Assess the morphology of the red blood cells.
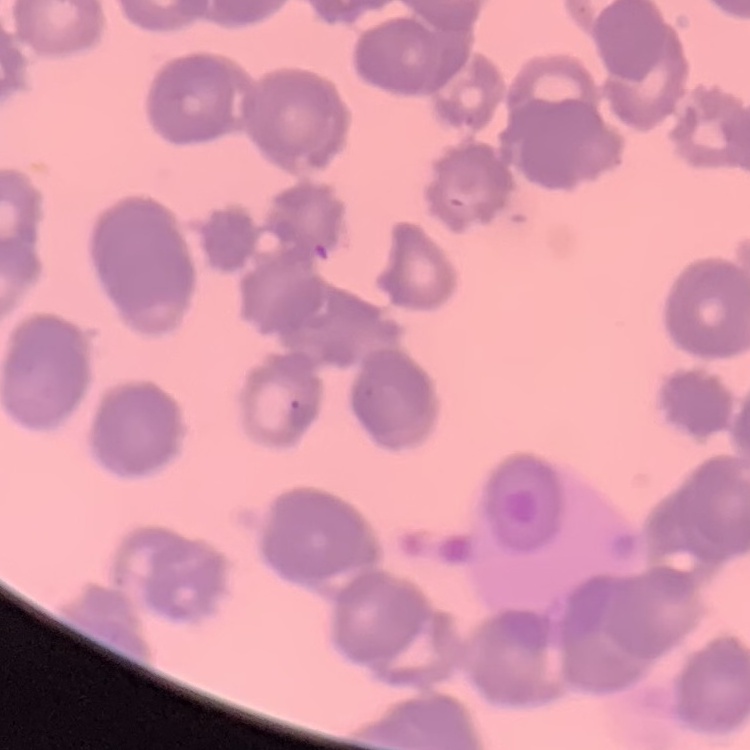
Rouleaux formation.

preparation: thin blood smear
image_type: one tile cut from a larger photomicrograph
stain: Field's or Giemsa